Give the position of every Plasmodium parasite visible.
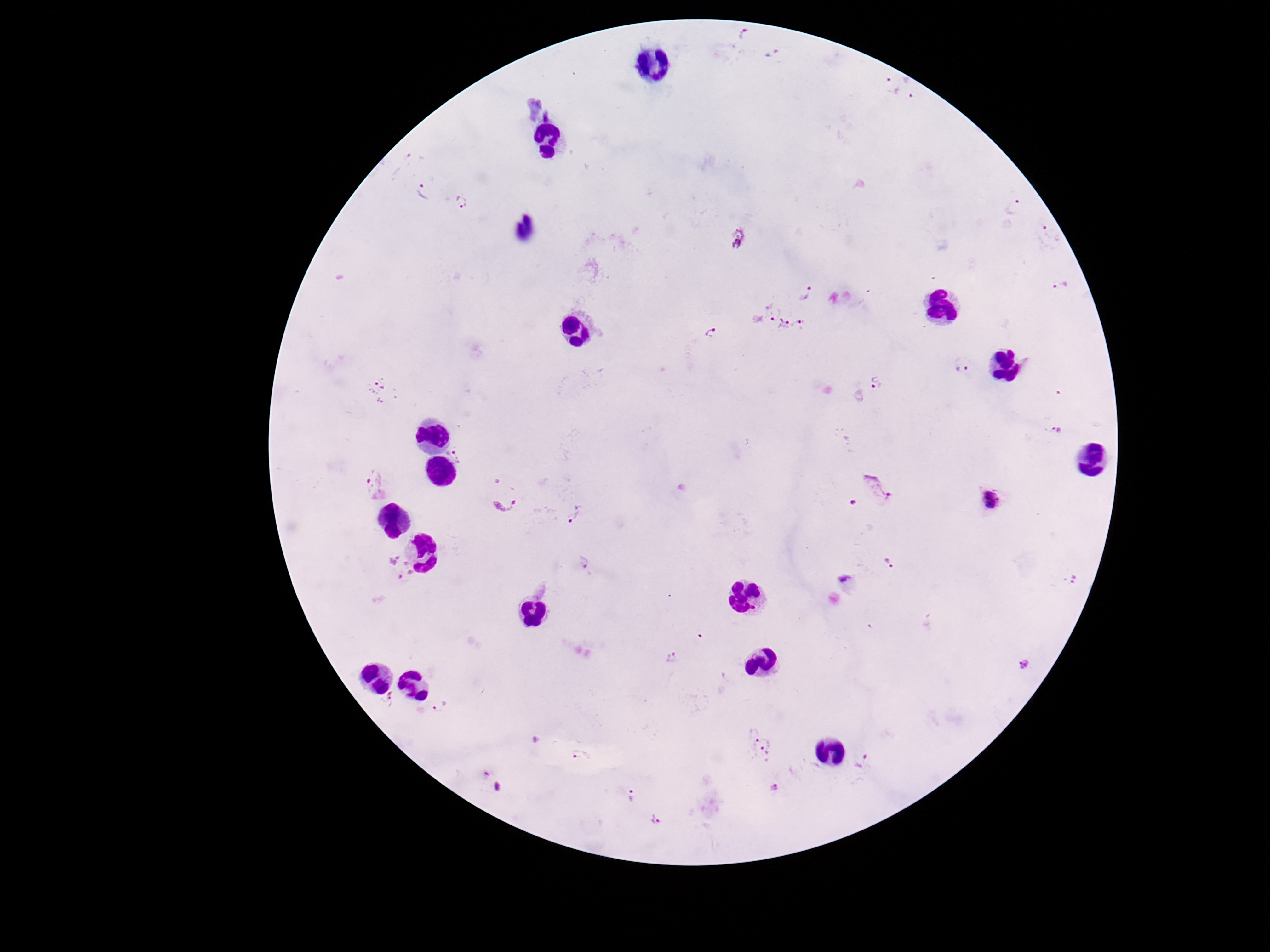
Approximate object centers, in pixels from the top-left corner.
Plasmodium parasites: (x=743, y=35), (x=775, y=53), (x=890, y=85), (x=912, y=90), (x=549, y=114), (x=423, y=190), (x=460, y=203), (x=1014, y=208), (x=739, y=236), (x=1051, y=236), (x=1061, y=288), (x=809, y=292), (x=769, y=311), (x=783, y=326), (x=801, y=326), (x=711, y=333), (x=962, y=369), (x=875, y=382), (x=378, y=391), (x=1058, y=430), (x=457, y=454), (x=376, y=485), (x=876, y=488), (x=502, y=494), (x=990, y=502), (x=854, y=504), (x=573, y=514), (x=888, y=562), (x=586, y=563), (x=400, y=570), (x=1074, y=579), (x=844, y=582), (x=672, y=657), (x=1023, y=664), (x=391, y=699), (x=439, y=706), (x=536, y=740), (x=759, y=744), (x=582, y=757), (x=863, y=763), (x=486, y=772), (x=497, y=787), (x=774, y=787), (x=631, y=795), (x=654, y=819).

stain = Giemsa
magnification = 100x
patient malaria status = infected
field of view = one from this slide
capture = smartphone camera through the microscope eyepiece
image size = 1270×952 pixels
preparation = thick blood smear